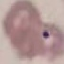

Summary:
  - Result: no malaria parasites seen
  - Stain: Giemsa
  - Capture: smartphone through the microscope eyepiece
  - Preparation: thin blood smear
  - Image type: automatically extracted cell patch, resized to 64 × 64 pixels